Give the position of every leukocyte visible.
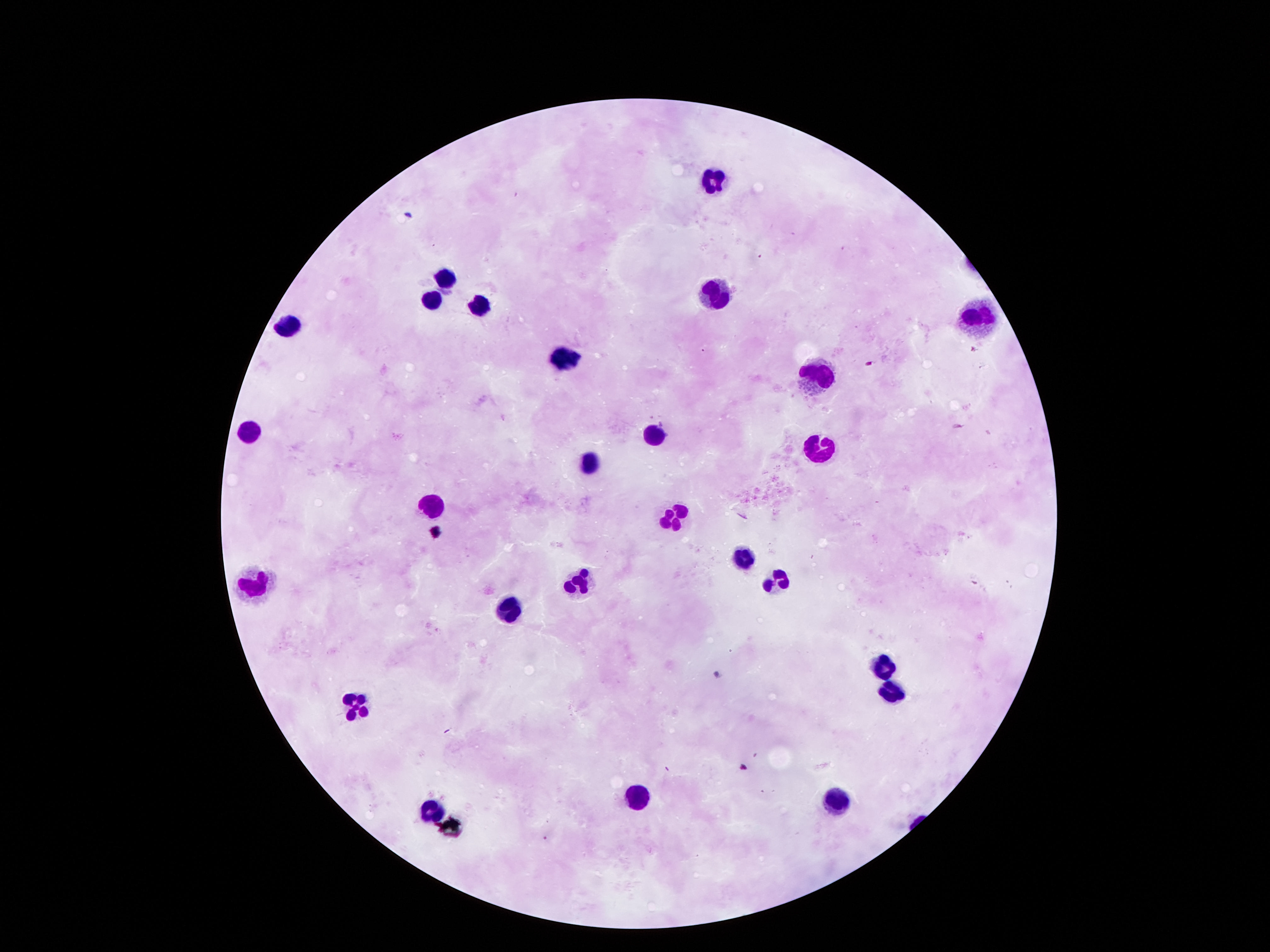
Approximate centers as (x, y) in pixels.
Leukocytes: (712, 179), (446, 275), (715, 296), (428, 300), (482, 305), (984, 312), (289, 327), (568, 353), (823, 378), (251, 433), (656, 433), (822, 449), (589, 460), (430, 508), (675, 517), (739, 558), (779, 579), (579, 582), (256, 585), (510, 609), (888, 664), (895, 694), (353, 701), (637, 793), (836, 797), (430, 810).

Giemsa-stained preparation. Patient malaria status: negative. Photographed through the microscope eyepiece with a smartphone camera. Thick blood film. One field from this slide. Image is 1270×952 pixels. 100x magnification.